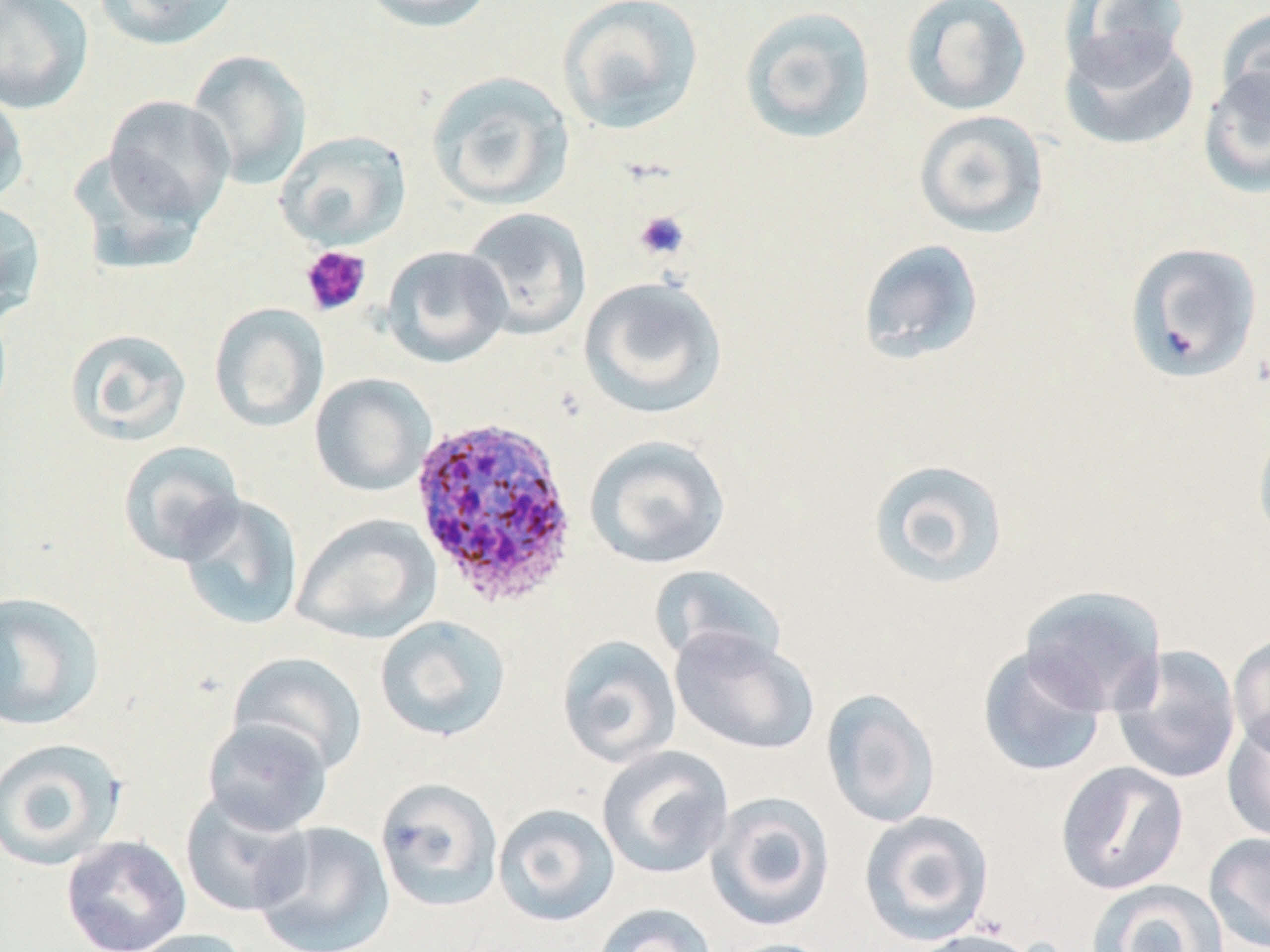 Approximate bounding boxes as (x1,y1)-(x2,y2) corner pairs in pixels. Uninfected red blood cell locations: (0,0)-(94,115), (93,0)-(242,51), (358,0)-(498,33), (557,0)-(704,135), (900,0)-(1032,117), (1056,0)-(1194,84), (738,6)-(876,146), (1217,7)-(1270,125), (1059,30)-(1199,152), (187,49)-(311,189), (1198,65)-(1270,199), (425,71)-(575,211), (0,88)-(29,206), (103,95)-(235,226), (913,110)-(1050,238), (275,130)-(411,250), (69,150)-(208,276), (0,198)-(46,323), (459,206)-(592,340), (856,239)-(985,366), (1123,241)-(1263,384), (381,244)-(513,368), (578,275)-(729,419), (209,302)-(329,433), (65,327)-(193,445), (309,373)-(436,497), (1253,422)-(1270,547), (584,435)-(732,570), (117,440)-(246,566), (866,457)-(1010,590), (175,493)-(304,631), (292,513)-(441,643), (649,564)-(787,672), (1019,585)-(1167,715), (0,590)-(106,731), (374,615)-(511,742), (669,627)-(820,755), (1228,632)-(1270,758), (556,635)-(682,769), (1109,644)-(1242,785), (977,645)-(1109,778), (228,651)-(368,776), (821,688)-(941,829), (1222,714)-(1270,844), (201,717)-(333,837), (0,737)-(128,872), (596,745)-(734,880), (1056,761)-(1188,894), (375,777)-(503,912), (179,788)-(313,919), (705,791)-(836,932), (493,803)-(620,927), (858,810)-(995,946), (251,821)-(395,952), (1203,831)-(1270,952), (61,834)-(192,952), (1087,879)-(1229,952), (592,902)-(718,952), (126,928)-(256,952), (903,928)-(1043,952), (716,938)-(842,952). Plasmodium ovale-infected red blood cell locations: (407,414)-(580,607). Platelet locations: (633,210)-(690,262), (300,245)-(371,317). Slide-level diagnosis: Plasmodium ovale. Thin blood smear. 1000x magnification. Light microscopy. Single field of view. Image is 1270×952 pixels. May-Grünwald-Giemsa stain.